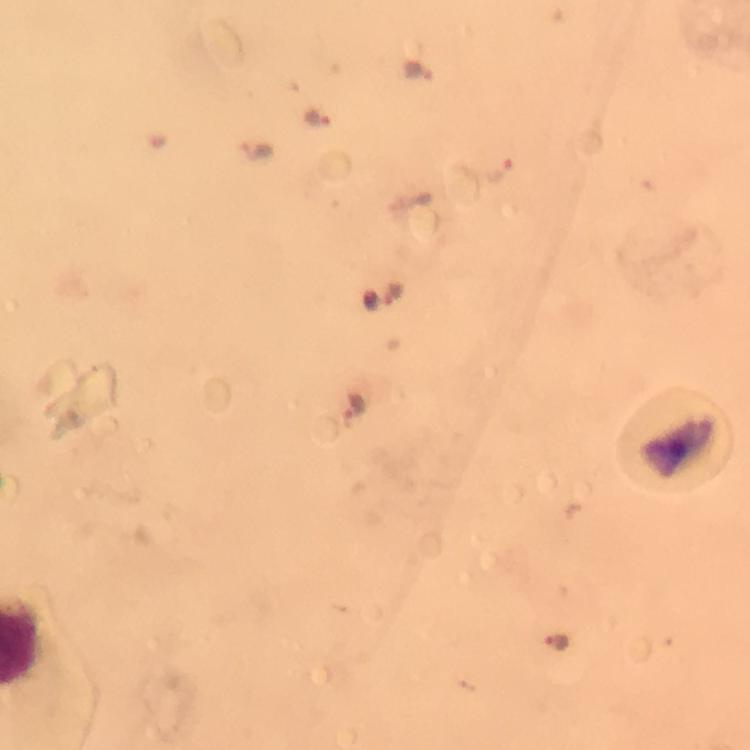

Approximate centers as [x, y] in pixels.
Summary:
  - Plasmodium parasite locations: [419, 71], [317, 117], [498, 168], [393, 294], [355, 408], [557, 642]
  - Capture: smartphone camera through the microscope
  - Image size: 750×750 pixels
  - Immersion oil: applied
  - Context: from a malaria diagnostic workup
  - Stain: Giemsa
  - Preparation: thick smear
  - Cropped from: one field of view
  - Magnification: 100x